Classify this cell by malaria status.
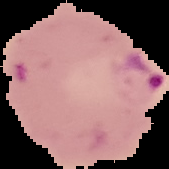

It is parasitized.

Image is 169×169 pixels. From a thin blood smear. Segmented cell region on a black background.